Point out each Plasmodium parasite.
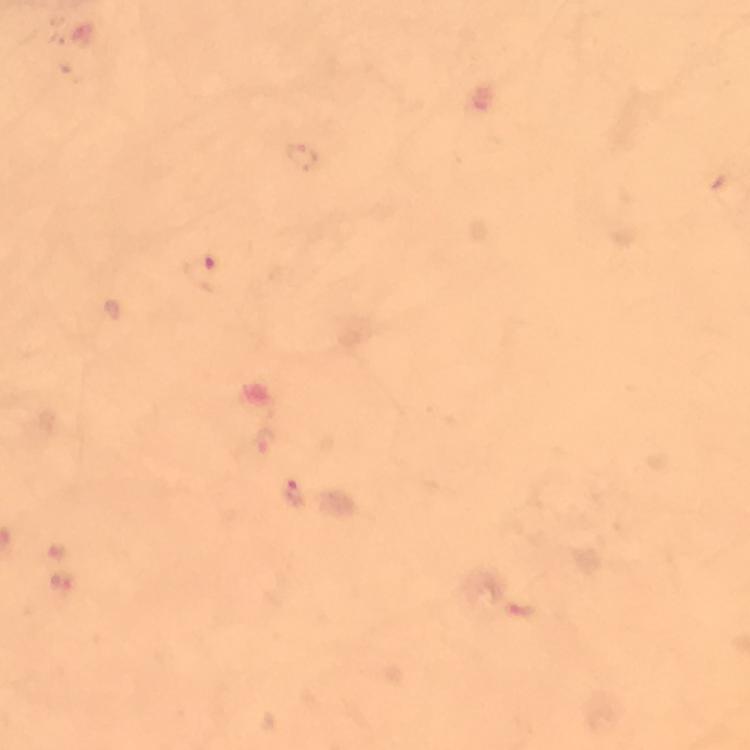

Approximate centers as {x, y} in pixels.
Plasmodium parasites: {206, 272}, {295, 493}.

context = from a malaria diagnostic workup
image size = 750×750 pixels
capture = smartphone camera through the microscope
magnification = 100x
cropped from = a single field of view
immersion oil = used
preparation = thick smear
stain = Giemsa